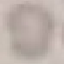 Malaria status: uninfected. Cell patch, automatically extracted from a larger field of view and resized to 64 × 64 pixels. Thin smear of blood. Photographed with a smartphone camera at the microscope eyepiece. Giemsa stain.